Give a bounding box for every leukocyte visible.
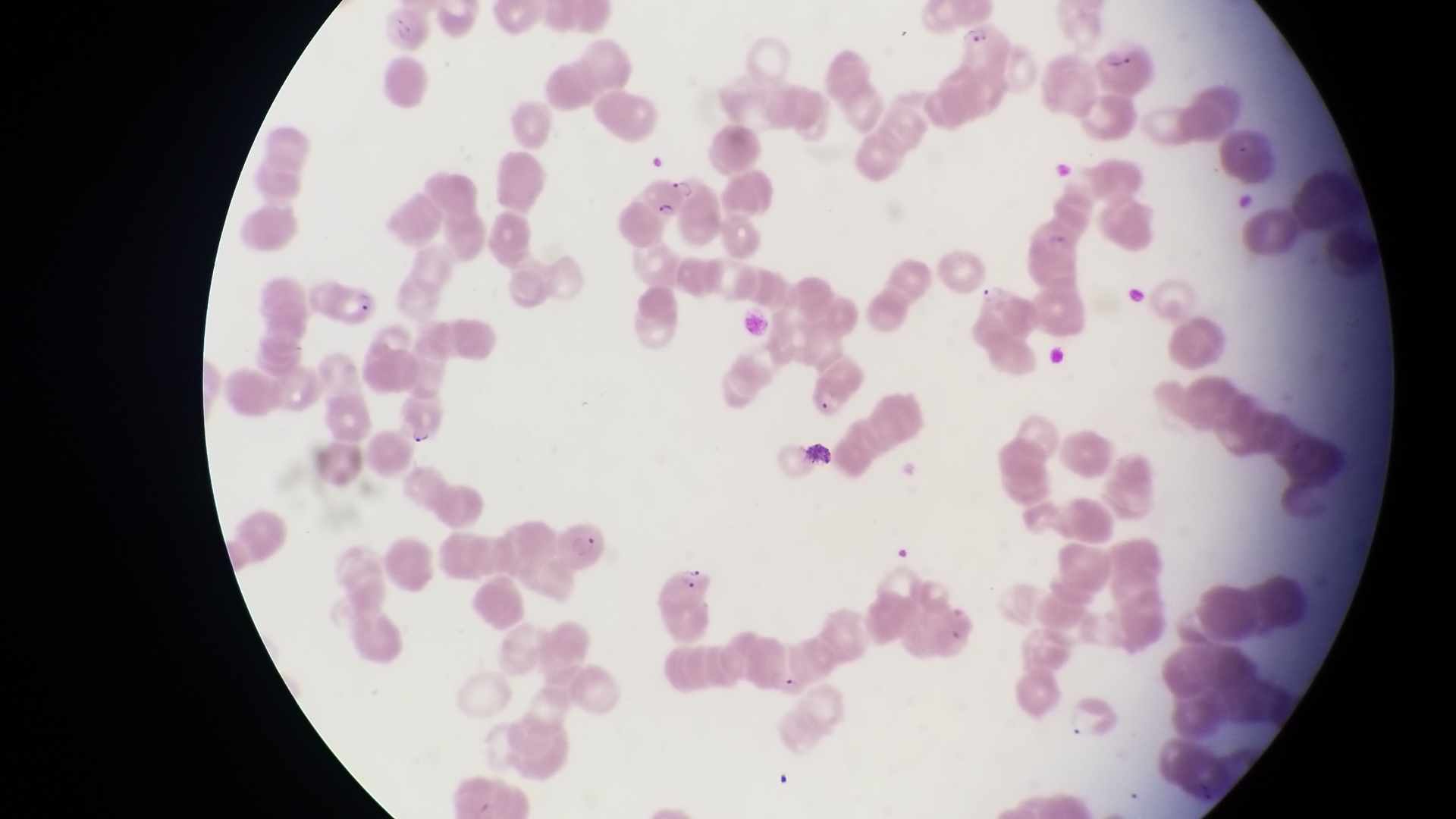
No leukocytes observed.

Approximate bounding boxes as [left, top, right, bottom] in pixels. Parasitised red blood cell locations: [639, 172, 700, 217], [320, 285, 387, 331], [391, 400, 452, 445], [555, 518, 611, 576], [653, 565, 725, 614]. Trophozoite locations: [974, 280, 1006, 307]. Thin blood film. Collected in Uganda. Photographed through the eyepiece of an Olympus CX-23 microscope with a smartphone camera. One field of view. Magnification of 1000x. Image is 1456×819 pixels.